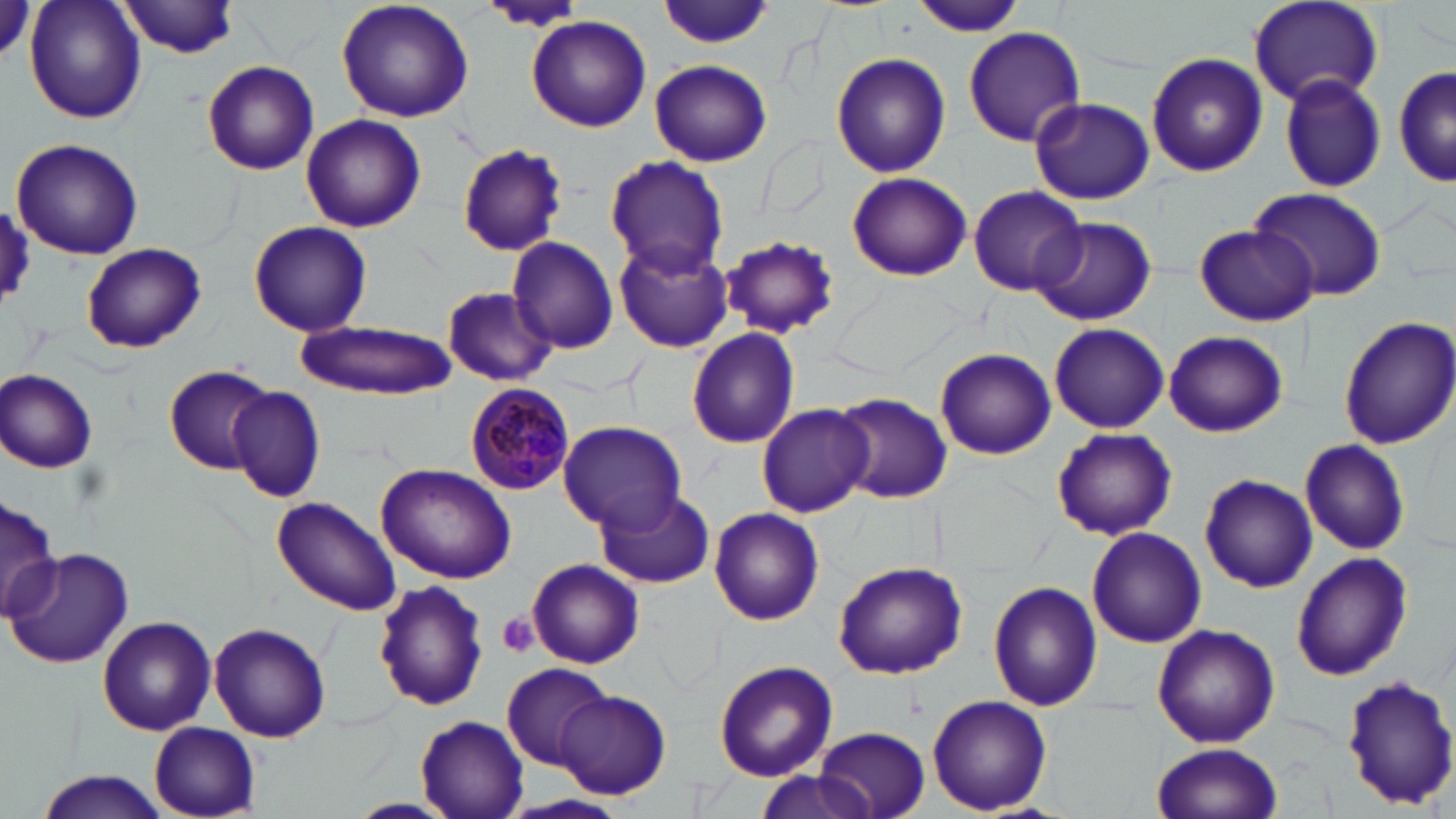
Summary:
  - Coordinate format: approximate bounding boxes as (x1, y1, x2, y2) in pixels
  - Platelet locations: (496, 612, 539, 658)
  - Uninfected red blood cell locations: (26, 0, 146, 123), (120, 0, 242, 58), (336, 0, 475, 123), (654, 1, 774, 49), (913, 2, 1027, 39), (1247, 2, 1384, 109), (526, 15, 652, 132), (961, 26, 1086, 148), (830, 52, 951, 178), (1145, 53, 1268, 177), (203, 59, 319, 175), (649, 60, 773, 167), (1393, 64, 1455, 190), (1279, 73, 1387, 193), (1028, 97, 1155, 204), (300, 114, 426, 232), (12, 139, 144, 260), (456, 143, 568, 256), (603, 155, 730, 277), (846, 172, 974, 280), (968, 183, 1088, 297), (1246, 186, 1388, 304), (0, 199, 32, 308), (1030, 216, 1154, 325), (248, 221, 372, 336), (1196, 224, 1318, 325), (721, 235, 840, 338), (506, 237, 620, 356), (613, 238, 734, 354), (81, 243, 206, 353), (441, 288, 556, 387), (1334, 314, 1456, 450), (298, 321, 456, 396), (1049, 322, 1169, 433), (686, 328, 801, 449), (1164, 330, 1288, 438), (936, 346, 1056, 460), (164, 364, 276, 472), (1, 369, 99, 473), (229, 387, 326, 504), (833, 392, 952, 503), (755, 404, 873, 518), (557, 420, 686, 532), (1051, 427, 1177, 541), (1299, 438, 1409, 557), (377, 463, 518, 583), (1200, 473, 1318, 593), (595, 488, 717, 589), (0, 495, 60, 624), (271, 496, 402, 618), (708, 506, 825, 625), (1085, 526, 1207, 648), (4, 549, 135, 669), (1290, 551, 1413, 683), (528, 559, 645, 669), (833, 560, 968, 680), (373, 577, 488, 713), (988, 581, 1102, 712), (97, 617, 215, 733), (208, 623, 330, 742), (1152, 624, 1280, 749), (712, 660, 838, 781), (502, 662, 614, 770), (1340, 675, 1456, 810), (555, 688, 672, 800), (927, 694, 1052, 816), (415, 715, 530, 819), (149, 723, 261, 817), (812, 726, 930, 819), (1152, 743, 1283, 819), (753, 770, 875, 819), (35, 771, 169, 819), (347, 798, 460, 819)
  - Plasmodium malariae-infected red blood cell locations: (466, 381, 575, 495)
  - Slide-level diagnosis: Plasmodium malariae
  - Preparation: thin blood film
  - Stain: May-Grünwald-Giemsa
  - Modality: optical microscopy
  - Image size: 1456×819 pixels
  - Field of view: single
  - Magnification: 1000x